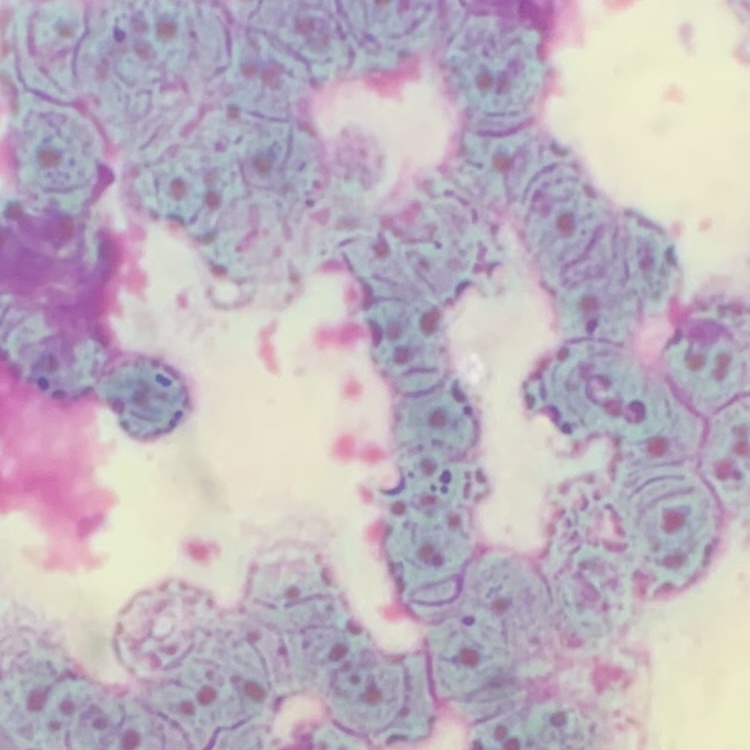

erythrocyte morphology = rouleaux formation
stain = Field's or Giemsa
image type = square crop of a larger photomicrograph
preparation = thin peripheral smear